Report the malaria status of this cell.
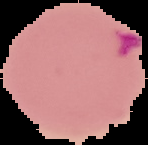
It is parasitized.

{
  "image_type": "segmented cell region on a black background",
  "image_size": "148×145 pixels",
  "preparation": "thin blood film"
}